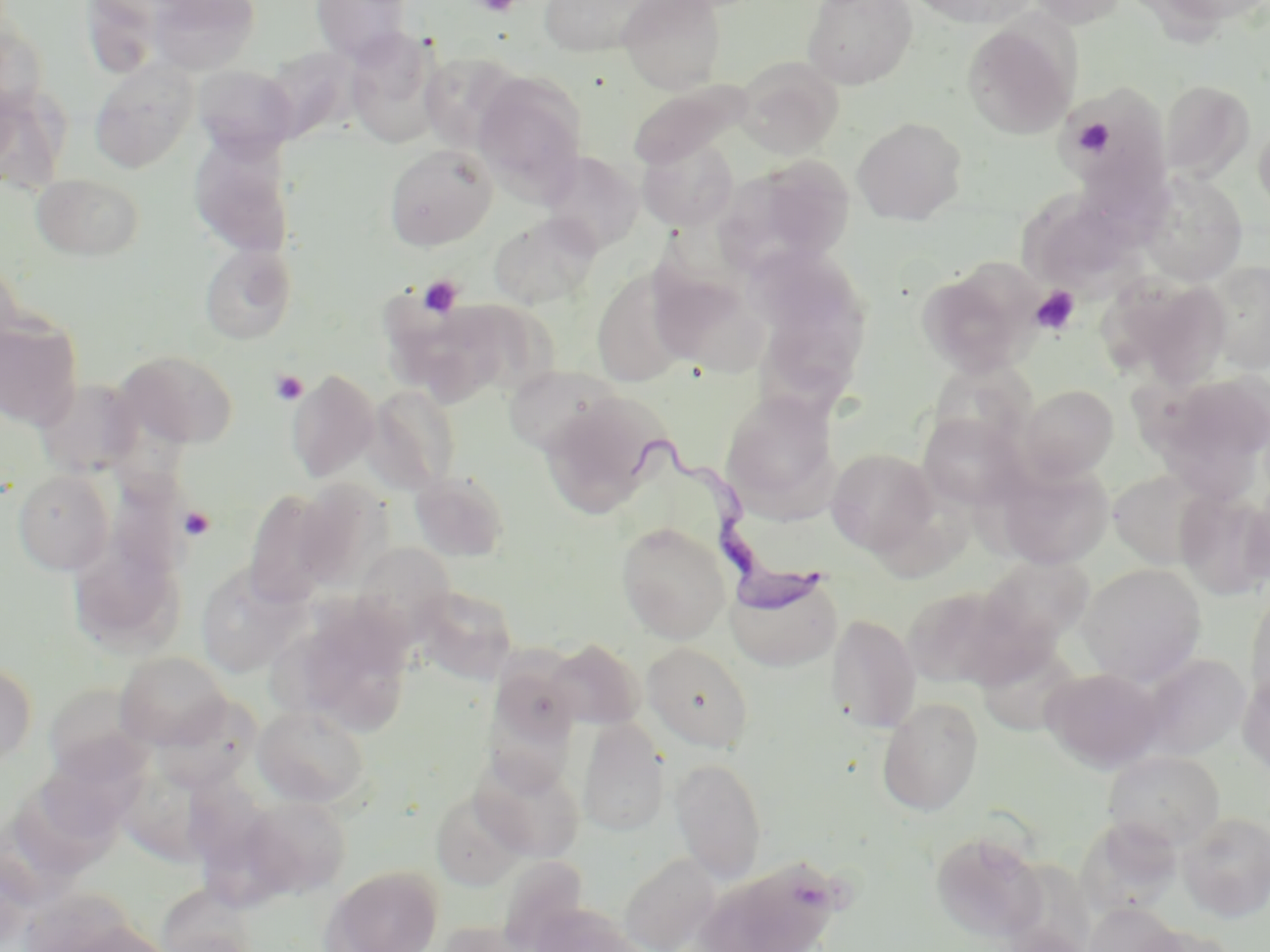
Summary:
  - Coordinate format: approximate bounding boxes as (x1,y1)-(x2,y2) corner pairs in pixels
  - Uninfected red blood cell locations: (148,0)-(261,74), (310,0)-(413,62), (539,0)-(652,56), (618,0)-(726,93), (802,0)-(918,90), (907,0)-(1040,28), (1024,0)-(1128,28), (1153,0)-(1270,26), (80,1)-(163,79), (961,19)-(1079,139), (0,22)-(50,117), (343,30)-(447,150), (418,53)-(525,153), (736,58)-(844,159), (89,61)-(198,172), (193,65)-(297,159), (473,71)-(588,201), (1158,80)-(1255,181), (628,81)-(751,171), (0,84)-(69,193), (1060,84)-(1171,202), (853,117)-(967,225), (1253,117)-(1270,219), (189,132)-(296,258), (638,137)-(738,231), (384,143)-(498,251), (540,151)-(643,255), (725,156)-(857,274), (1139,171)-(1248,287), (32,173)-(144,261), (1018,193)-(1140,294), (489,212)-(601,309), (199,242)-(297,345), (0,258)-(25,363), (1203,260)-(1269,374), (917,263)-(1039,378), (648,266)-(764,373), (592,267)-(694,387), (755,274)-(873,407), (1116,277)-(1235,390), (391,295)-(539,406), (0,315)-(84,430), (116,349)-(239,449), (928,360)-(1035,452), (503,364)-(625,458), (286,368)-(380,483), (1150,370)-(1270,485), (366,384)-(463,494), (1020,384)-(1119,479), (720,388)-(841,515), (539,392)-(670,519), (917,412)-(1026,511), (826,448)-(938,556), (993,462)-(1114,569), (1108,468)-(1217,568), (13,469)-(115,576), (409,469)-(511,562), (294,479)-(395,592), (244,489)-(336,606), (1176,491)-(1270,599), (1241,494)-(1270,588), (616,522)-(731,643), (69,534)-(186,658), (351,542)-(457,641), (979,555)-(1095,652), (195,562)-(310,678), (1078,563)-(1206,686), (725,569)-(844,672), (902,584)-(1023,689), (414,585)-(518,684), (1246,585)-(1270,710), (276,601)-(418,739), (825,613)-(921,733), (973,638)-(1086,737), (546,639)-(645,730), (643,642)-(753,751), (115,651)-(231,750), (1137,652)-(1250,759), (0,662)-(37,768), (1041,667)-(1166,773), (1238,667)-(1270,776), (47,679)-(160,774), (153,694)-(262,791), (877,698)-(984,816), (253,704)-(371,808), (577,718)-(670,837), (43,748)-(156,837), (1103,750)-(1225,850), (470,751)-(586,862), (670,757)-(767,882), (185,763)-(291,868), (16,777)-(122,880), (430,789)-(529,890), (242,796)-(352,897), (1178,811)-(1270,922), (931,831)-(1046,943), (620,852)-(721,952), (711,859)-(845,951), (323,865)-(444,952), (1084,902)-(1184,952), (528,903)-(641,952), (437,919)-(535,952), (1136,923)-(1239,952)
  - Platelet locations: (474,0)-(520,16), (1072,117)-(1117,157), (418,276)-(463,319), (1030,286)-(1081,335), (269,368)-(308,406), (179,506)-(216,540)
  - Trypanosoma brucei locations: (621,439)-(832,617)
  - Slide-level diagnosis: Trypanosoma brucei
  - Stain: May-Grünwald-Giemsa
  - Modality: optical microscopy
  - Field of view: one of a larger specimen
  - Magnification: 1000x
  - Preparation: thin blood smear
  - Image size: 1270×952 pixels